Outline each Plasmodium parasite.
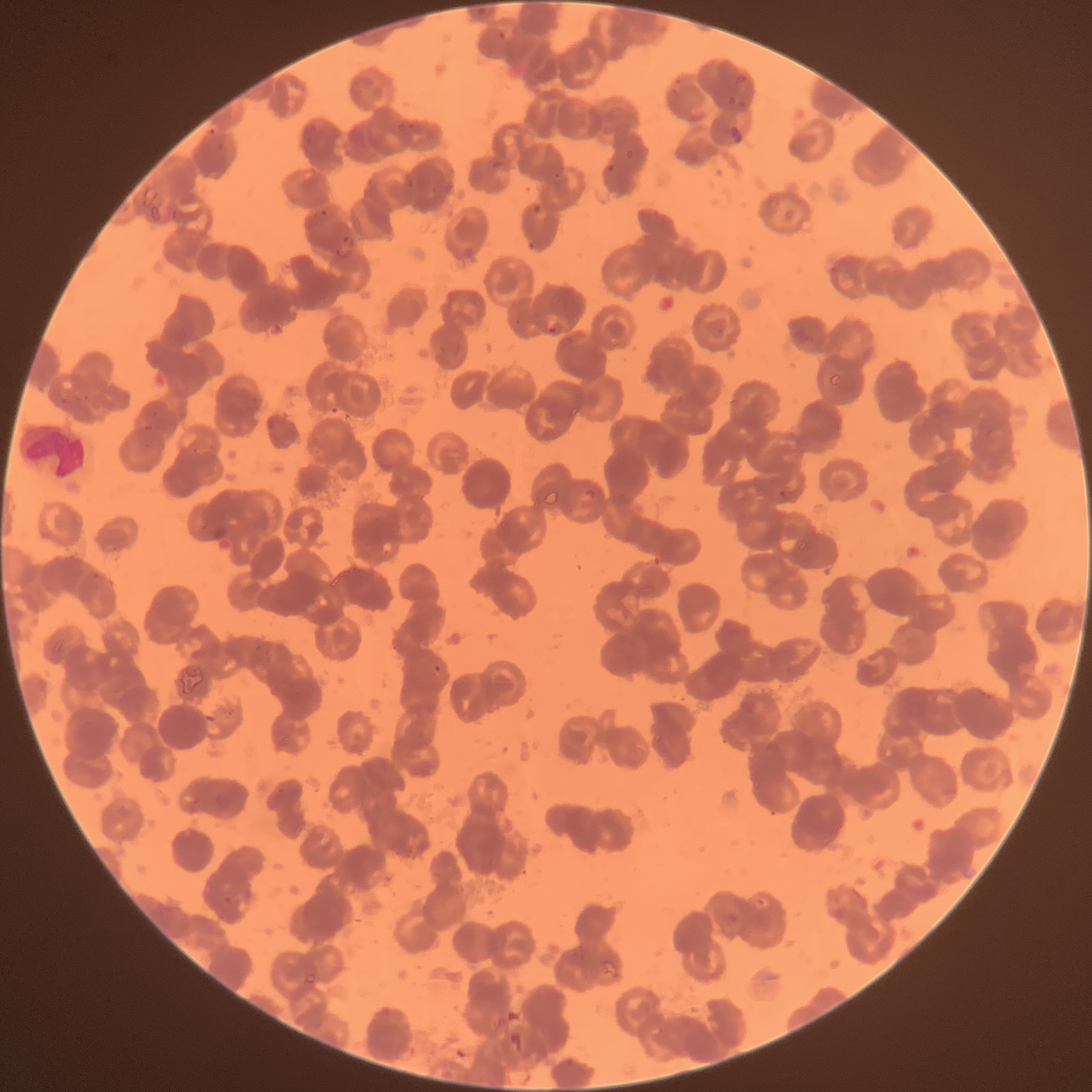

Approximate bounding boxes as (x1,y1)-(x2,y2) corner pairs in pixels.
Plasmodium parasites: (498,30)-(507,40), (407,122)-(421,130), (729,124)-(743,143), (208,128)-(218,135), (491,159)-(505,169), (606,163)-(617,175), (553,173)-(562,179), (405,178)-(415,189), (532,203)-(543,216), (317,208)-(329,219), (336,233)-(355,261), (527,240)-(538,253), (546,319)-(563,337), (582,489)-(597,503), (779,490)-(801,503), (91,572)-(101,580), (432,663)-(443,675), (224,896)-(233,905), (753,896)-(770,913), (728,912)-(742,926).

image size = 1092×1092 pixels
red blood cell morphology = rouleaux formation
modality = optical microscopy
preparation = thin blood smear